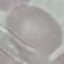

{
  "result": "no malaria parasites seen",
  "preparation": "thin blood film",
  "image_type": "cell patch, automatically extracted from a larger field of view and resized to 64 × 64 pixels",
  "capture": "smartphone camera at the microscope eyepiece",
  "stain": "Giemsa"
}